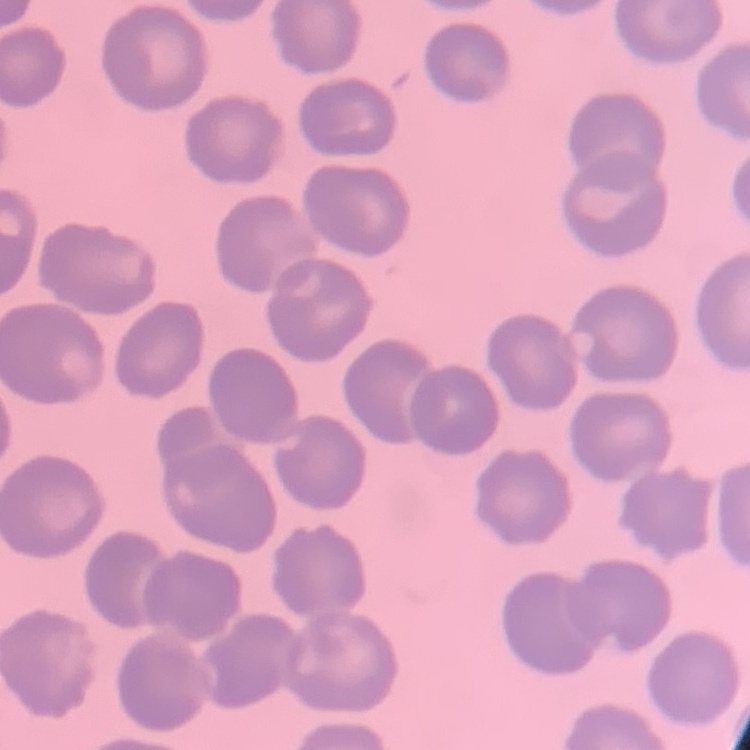
Summary:
  - Red blood cell morphology: no rouleaux formation
  - Stain: Field's or Giemsa
  - Preparation: thin blood film
  - Image type: one tile cut from a larger photomicrograph